State the blood parasite species.
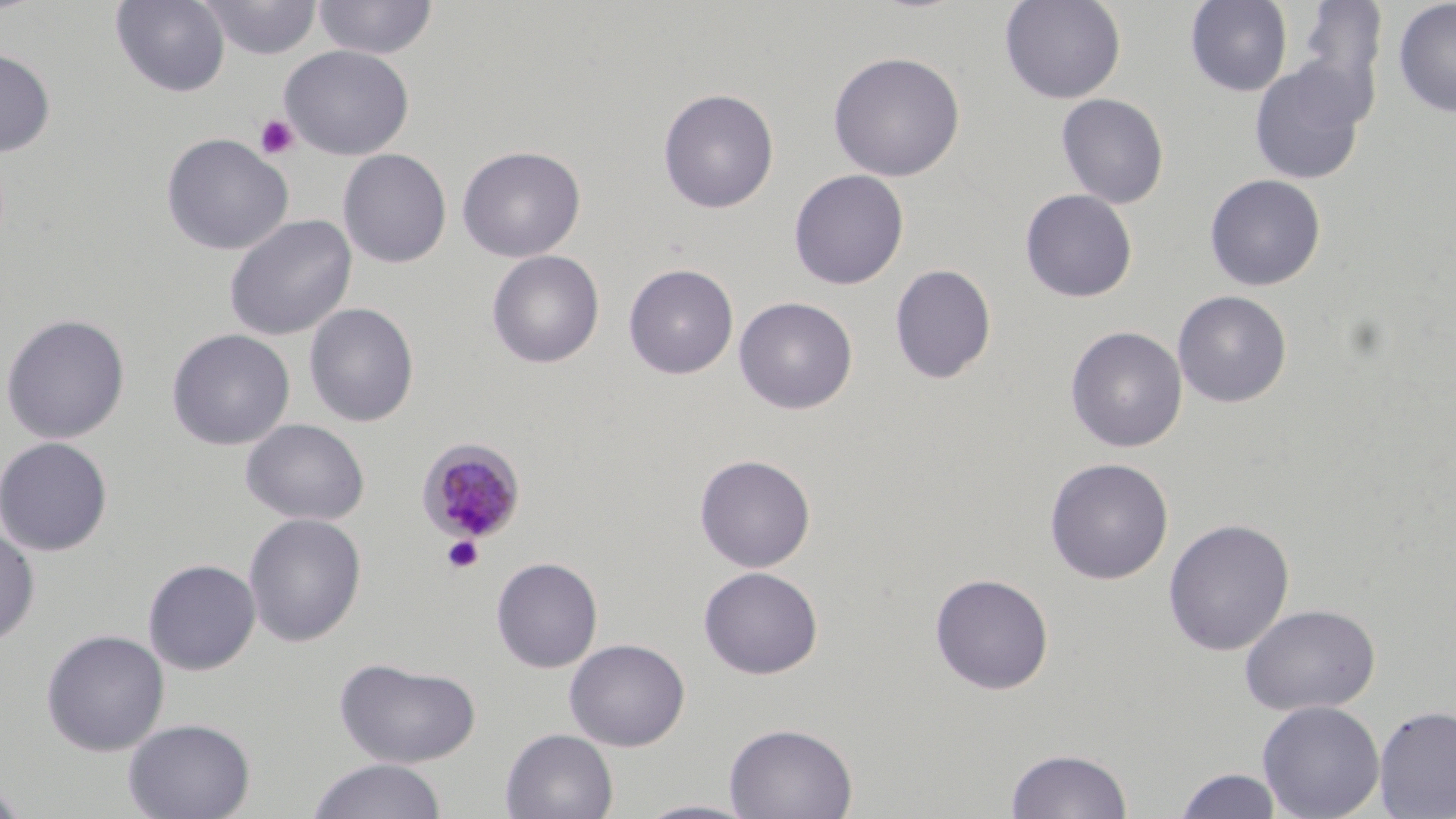
Plasmodium malariae.

Approximate bounding boxes as named x1/y1/x2/y2 corners in pixels. Uninfected red blood cell locations: (x1=110, y1=0, x2=230, y2=97), (x1=199, y1=0, x2=322, y2=60), (x1=313, y1=0, x2=438, y2=60), (x1=999, y1=0, x2=1126, y2=104), (x1=1185, y1=0, x2=1293, y2=96), (x1=1297, y1=0, x2=1388, y2=115), (x1=1392, y1=0, x2=1456, y2=118), (x1=279, y1=44, x2=414, y2=160), (x1=0, y1=47, x2=56, y2=157), (x1=827, y1=51, x2=965, y2=182), (x1=1248, y1=61, x2=1367, y2=185), (x1=658, y1=88, x2=779, y2=214), (x1=1056, y1=93, x2=1169, y2=208), (x1=161, y1=132, x2=294, y2=255), (x1=457, y1=146, x2=585, y2=262), (x1=338, y1=149, x2=452, y2=268), (x1=788, y1=169, x2=909, y2=290), (x1=1204, y1=173, x2=1326, y2=291), (x1=1020, y1=188, x2=1137, y2=303), (x1=224, y1=214, x2=357, y2=341), (x1=486, y1=250, x2=605, y2=368), (x1=623, y1=263, x2=739, y2=380), (x1=889, y1=263, x2=996, y2=384), (x1=1172, y1=290, x2=1292, y2=407), (x1=734, y1=296, x2=858, y2=414), (x1=303, y1=302, x2=419, y2=427), (x1=1, y1=313, x2=131, y2=445), (x1=1065, y1=326, x2=1187, y2=453), (x1=167, y1=328, x2=295, y2=450), (x1=240, y1=418, x2=369, y2=525), (x1=0, y1=436, x2=113, y2=556), (x1=694, y1=454, x2=816, y2=572), (x1=1044, y1=457, x2=1174, y2=584), (x1=243, y1=512, x2=367, y2=646), (x1=1163, y1=518, x2=1295, y2=656), (x1=0, y1=523, x2=40, y2=648), (x1=491, y1=556, x2=604, y2=673), (x1=142, y1=558, x2=262, y2=676), (x1=698, y1=566, x2=823, y2=679), (x1=930, y1=572, x2=1054, y2=694), (x1=1240, y1=603, x2=1380, y2=716), (x1=41, y1=629, x2=170, y2=756), (x1=564, y1=638, x2=690, y2=751), (x1=333, y1=657, x2=482, y2=768), (x1=1257, y1=699, x2=1385, y2=819), (x1=1373, y1=704, x2=1456, y2=818), (x1=123, y1=717, x2=255, y2=819), (x1=724, y1=721, x2=858, y2=819), (x1=500, y1=728, x2=619, y2=818), (x1=1005, y1=747, x2=1133, y2=819), (x1=306, y1=758, x2=448, y2=819), (x1=1173, y1=768, x2=1284, y2=818), (x1=0, y1=776, x2=30, y2=819), (x1=632, y1=799, x2=762, y2=818). Platelet locations: (x1=254, y1=114, x2=299, y2=161), (x1=442, y1=535, x2=484, y2=573). Plasmodium malariae-infected red blood cell locations: (x1=417, y1=438, x2=526, y2=542). Image is 1456×819 pixels. Thin blood film. One field of a larger specimen. May-Grünwald-Giemsa stain. 1000x magnification. Optical microscopy.